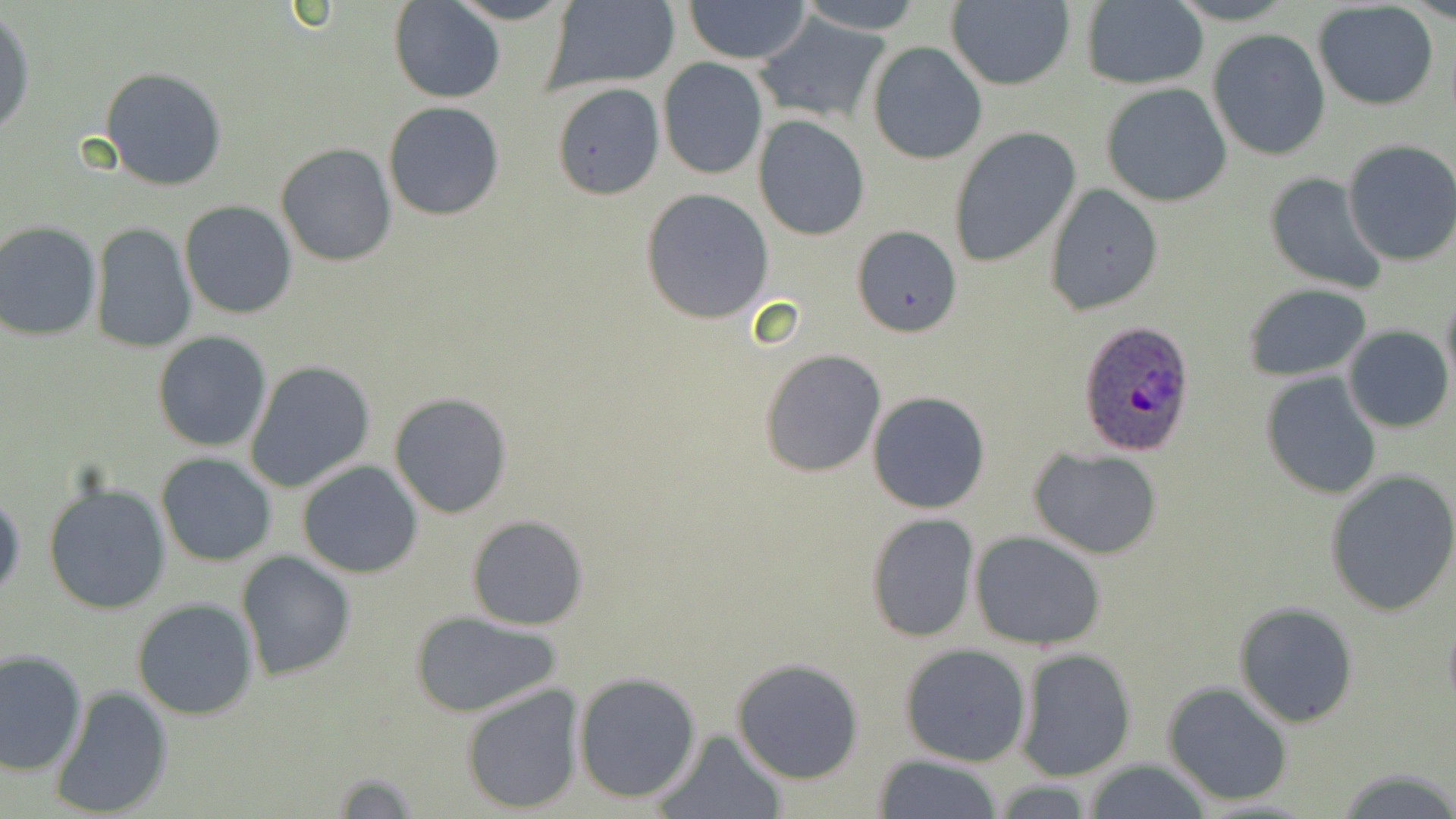
Approximate bounding boxes as [x1, y1, x2, y2] in pixels. Plasmodium ovale-infected red blood cell locations: [1077, 321, 1198, 458]. Uninfected red blood cell locations: [445, 0, 577, 25], [541, 0, 680, 92], [682, 0, 813, 64], [789, 0, 929, 34], [390, 1, 505, 103], [945, 1, 1075, 90], [1079, 1, 1208, 89], [1312, 2, 1440, 110], [0, 12, 36, 138], [753, 16, 886, 125], [1207, 29, 1331, 160], [868, 41, 988, 165], [657, 58, 767, 180], [100, 66, 229, 191], [551, 82, 670, 197], [1101, 83, 1232, 207], [383, 101, 505, 221], [753, 116, 870, 242], [947, 128, 1081, 268], [1341, 139, 1456, 267], [275, 144, 397, 266], [1264, 171, 1388, 294], [1044, 184, 1163, 316], [641, 188, 774, 324], [179, 200, 300, 320], [0, 219, 102, 341], [90, 221, 197, 353], [849, 223, 962, 337], [1241, 284, 1371, 381], [1440, 286, 1456, 396], [1344, 325, 1453, 433], [152, 331, 273, 453], [760, 348, 886, 477], [247, 359, 375, 492], [1259, 372, 1382, 499], [867, 389, 993, 514], [389, 391, 514, 520], [1028, 446, 1163, 559], [156, 454, 275, 567], [297, 460, 423, 578], [1323, 469, 1456, 617], [43, 480, 170, 616], [0, 490, 24, 602], [865, 513, 980, 643], [467, 515, 589, 631], [970, 530, 1106, 650], [237, 551, 355, 680], [132, 598, 259, 721], [1233, 600, 1359, 728], [409, 610, 564, 717], [899, 643, 1032, 766], [1, 649, 87, 775], [1017, 649, 1137, 781], [730, 658, 864, 786], [573, 671, 702, 804], [1162, 681, 1292, 806], [459, 682, 585, 814], [48, 684, 175, 818], [653, 728, 787, 818], [872, 755, 1008, 818], [1080, 759, 1213, 819], [1332, 764, 1456, 819], [319, 768, 427, 815]. Slide-level diagnosis: Plasmodium ovale. Optical microscopy. May-Grünwald-Giemsa-stained preparation. Single field of view. 1000x magnification. Image is 1456×819 pixels. Thin blood film.